Classify this cell by malaria status.
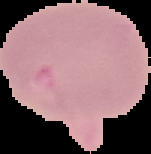

It is uninfected.

image size = 151×154 pixels
image type = segmented cell region on a black background
preparation = thin blood film